Give the extent of all uninfected red blood cells.
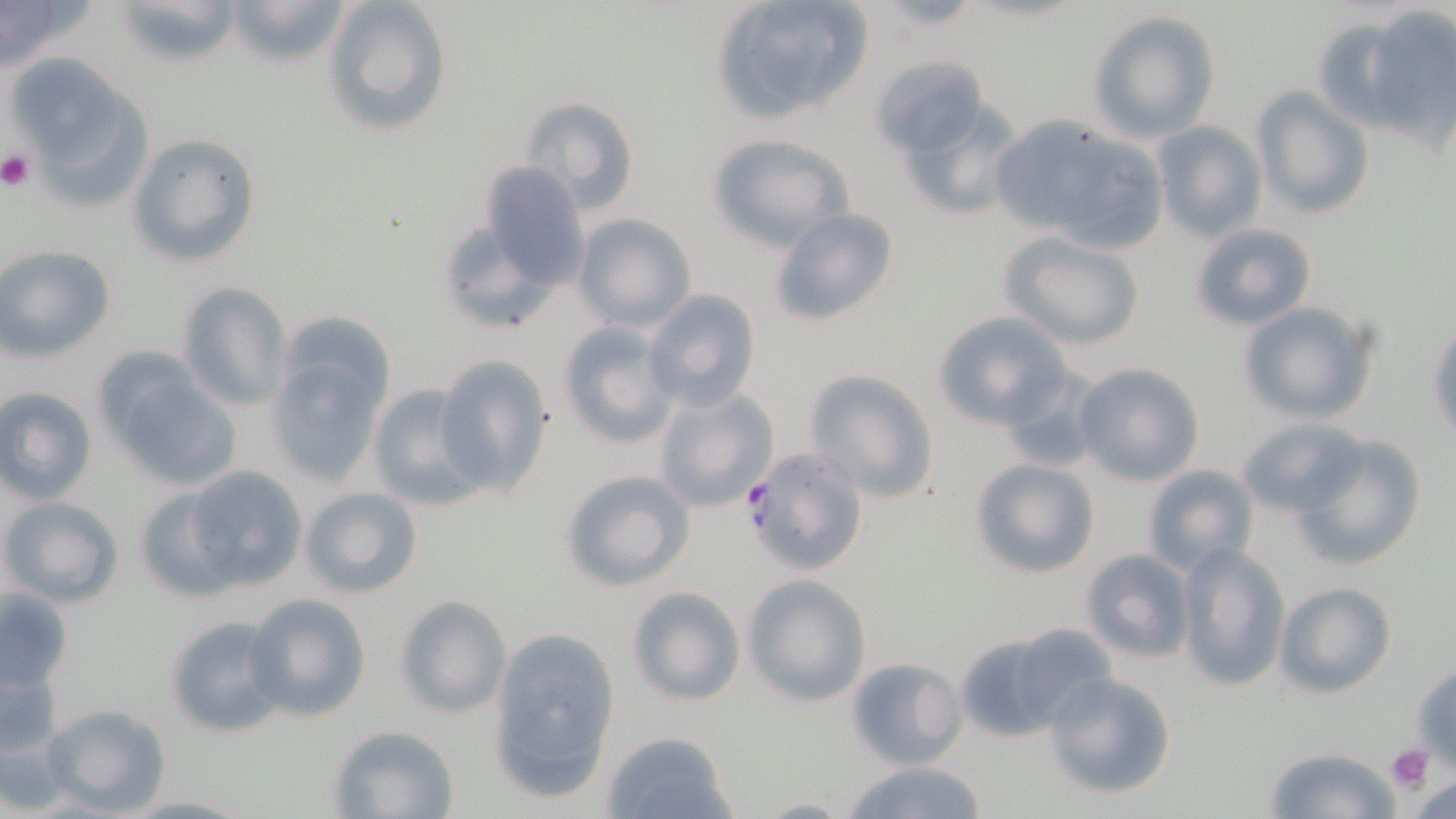
Approximate bounding boxes as [x1, y1, x2, y2] in pixels.
Uninfected red blood cells: [0, 0, 93, 73], [109, 0, 242, 68], [223, 0, 355, 68], [324, 0, 453, 136], [710, 0, 875, 122], [870, 1, 988, 31], [1360, 6, 1456, 136], [1088, 9, 1222, 143], [873, 56, 990, 158], [9, 57, 152, 206], [1250, 86, 1377, 221], [887, 92, 1027, 225], [519, 94, 643, 217], [988, 116, 1163, 251], [1150, 120, 1267, 243], [127, 132, 262, 267], [705, 132, 854, 250], [477, 162, 591, 288], [767, 207, 902, 326], [572, 212, 698, 332], [435, 217, 560, 335], [1189, 222, 1318, 331], [1003, 232, 1147, 349], [0, 244, 117, 361], [177, 280, 291, 412], [643, 288, 763, 411], [1238, 300, 1381, 425], [933, 310, 1072, 428], [1427, 319, 1456, 446], [556, 320, 681, 449], [265, 337, 393, 488], [433, 353, 554, 496], [1073, 360, 1205, 486], [989, 365, 1104, 475], [104, 366, 239, 493], [802, 367, 942, 505], [367, 382, 487, 510], [653, 384, 780, 514], [0, 385, 98, 504], [1237, 418, 1365, 517], [1291, 433, 1425, 569], [968, 457, 1101, 579], [1139, 464, 1261, 576], [181, 465, 307, 593], [560, 467, 696, 591], [134, 486, 241, 601], [299, 486, 423, 599], [1, 495, 126, 610], [1173, 543, 1290, 688], [1081, 548, 1195, 661], [742, 573, 873, 706], [1273, 581, 1397, 696], [624, 585, 746, 707], [1, 587, 74, 691], [245, 592, 373, 721], [395, 594, 511, 718], [166, 613, 293, 737], [487, 624, 624, 802], [952, 626, 1093, 742], [845, 655, 968, 769], [0, 656, 65, 761], [1410, 660, 1456, 768], [1043, 670, 1178, 800], [37, 703, 171, 816], [327, 723, 460, 817], [601, 729, 739, 818], [1262, 745, 1402, 819], [839, 758, 992, 819], [117, 793, 251, 817], [755, 795, 856, 817].

Platelet locations: [0, 150, 36, 190], [1386, 743, 1433, 793]. Plasmodium falciparum-infected red blood cell locations: [741, 444, 872, 576]. Slide-level diagnosis: Plasmodium falciparum. Captured at 1000x magnification. Image is 1456×819 pixels. Single field of view. May-Grünwald-Giemsa stain. Light microscopy. Thin blood smear.